Assess this cell for malaria.
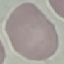

It is uninfected.

image_type: automatically extracted cell patch, resized to 64 × 64 pixels
preparation: thin blood smear
stain: Giemsa
capture: smartphone camera at the microscope eyepiece